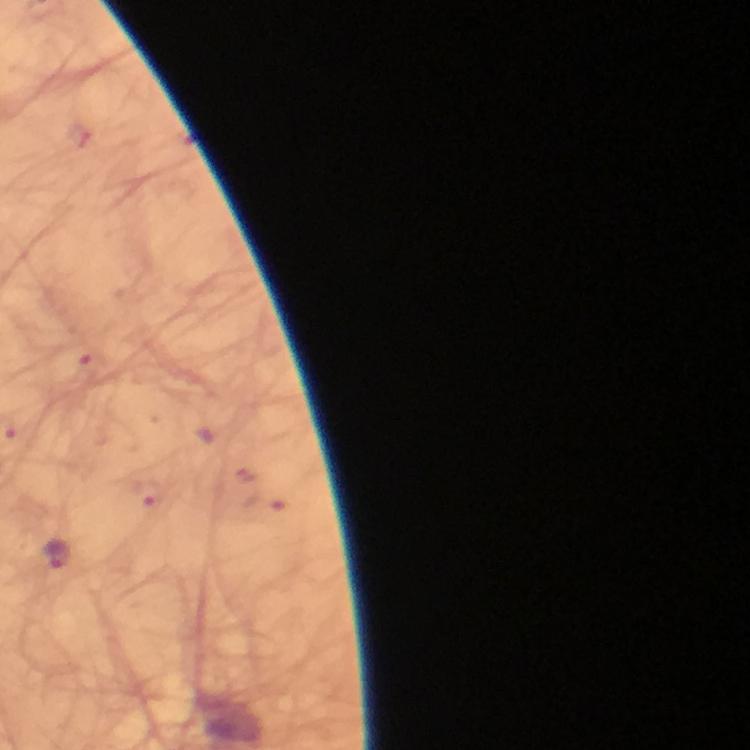 Approximate object centers, in pixels from the top-left corner. Plasmodium parasite locations: (x=57, y=555). Thick smear. A crop from one field of view. Immersion oil was used. Giemsa stain. Image is 750×750 pixels. From a diagnostic examination for malaria. 100x magnification. Photographed with a smartphone mounted on the microscope.